Assess for Plasmodium parasites.
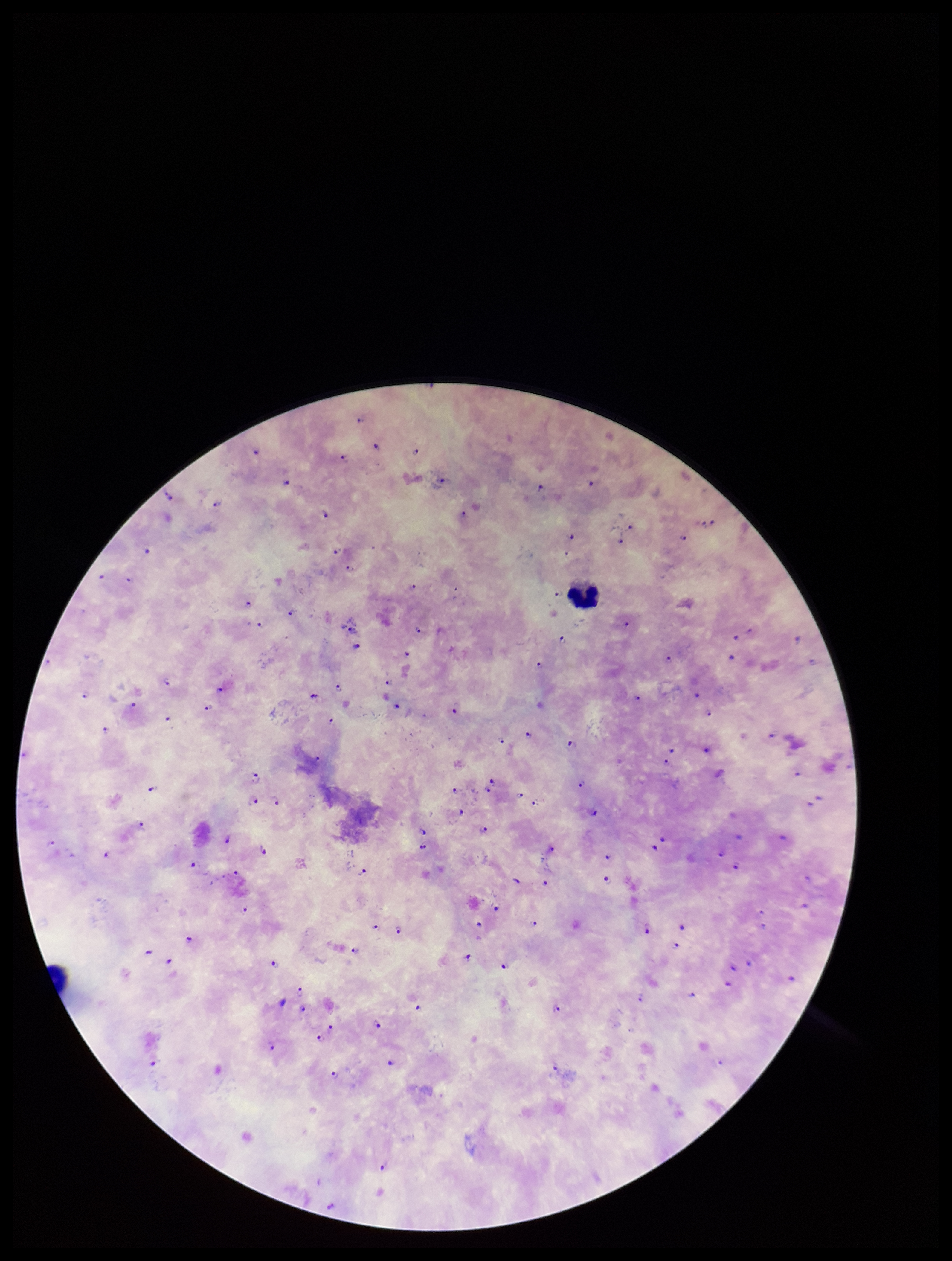
Seen.

capture = smartphone photograph through the microscope eyepiece
stain = Giemsa
species reported for this patient = Plasmodium falciparum
preparation = thick smear
parasite count = 103
image size = 952×1261 pixels
field of view = single
patient malaria status = positive
leukocyte count = 1